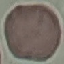 Malaria status: uninfected. Cell patch, automatically extracted from a larger field of view and resized to 64 × 64 pixels. Giemsa stain. Photographed with a smartphone camera at the microscope eyepiece. Thin blood film.